Identify the blood parasite species.
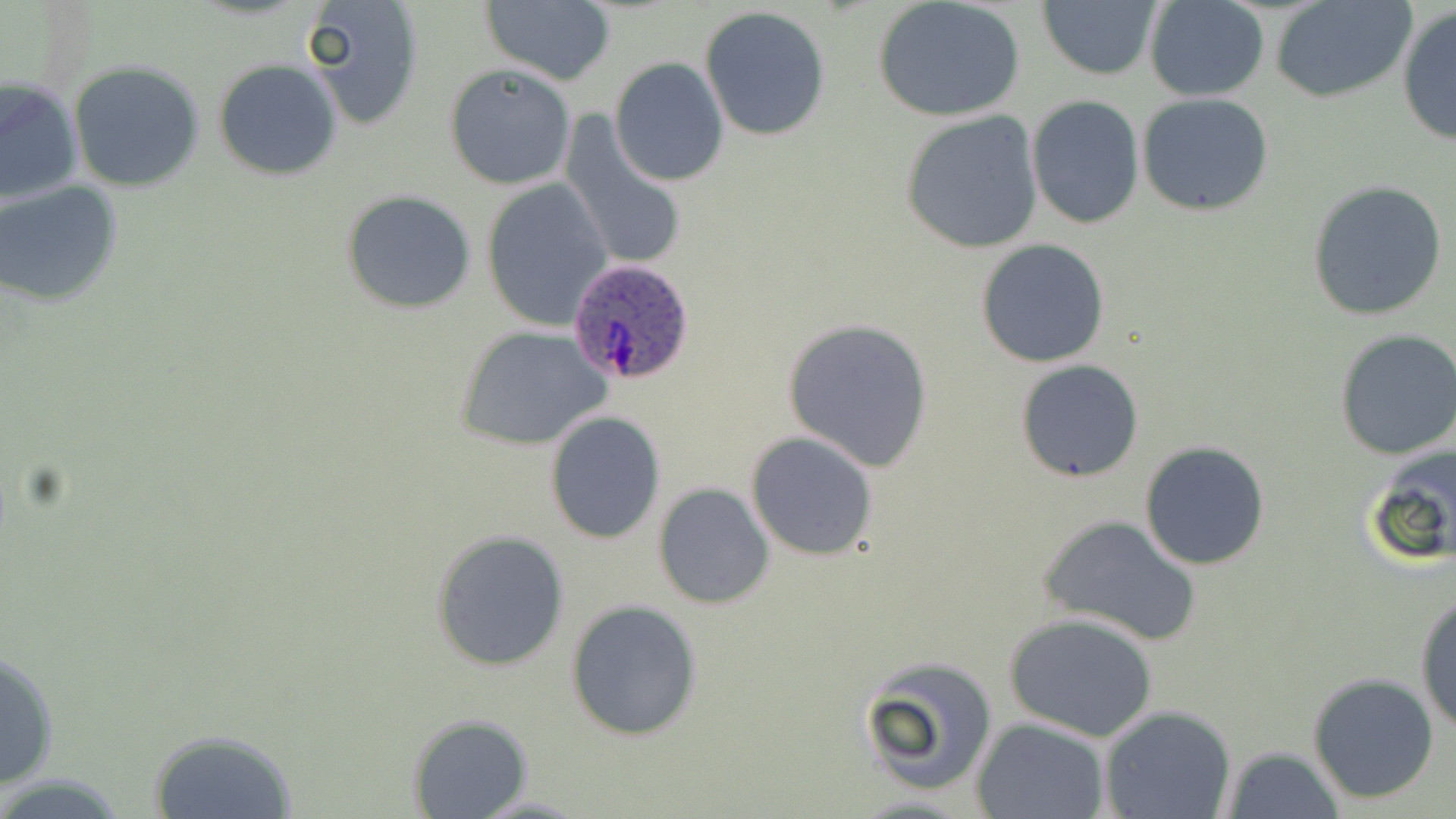

Plasmodium ovale.

Summary:
  - Coordinate format: approximate bounding boxes as [x1, y1, x2, y2] in pixels
  - Plasmodium ovale-infected red blood cell locations: [566, 257, 697, 386]
  - Uninfected red blood cell locations: [300, 0, 427, 131], [479, 0, 618, 87], [871, 0, 1027, 123], [1268, 0, 1420, 104], [1144, 1, 1271, 101], [1037, 2, 1161, 81], [699, 6, 832, 142], [1396, 7, 1456, 146], [610, 57, 729, 186], [213, 59, 342, 180], [68, 61, 205, 191], [444, 63, 579, 191], [0, 75, 84, 205], [1136, 91, 1275, 217], [1026, 97, 1145, 229], [899, 110, 1045, 253], [556, 112, 691, 276], [481, 178, 613, 330], [1305, 179, 1449, 321], [0, 180, 124, 309], [341, 189, 478, 315], [975, 238, 1110, 368], [782, 318, 934, 473], [454, 324, 611, 451], [1334, 330, 1456, 461], [1015, 359, 1143, 483], [544, 411, 667, 543], [745, 433, 879, 559], [1139, 441, 1272, 571], [1361, 442, 1456, 567], [653, 482, 776, 610], [1038, 514, 1204, 648], [430, 531, 570, 671], [1414, 591, 1456, 734], [566, 599, 704, 741], [1004, 612, 1158, 742], [1, 647, 60, 794], [858, 655, 998, 799], [1306, 671, 1439, 804], [1098, 705, 1238, 819], [406, 713, 532, 819], [973, 717, 1110, 819], [147, 728, 298, 818], [1219, 745, 1345, 819], [470, 793, 591, 817]
  - Image size: 1456×819 pixels
  - Magnification: 1000x
  - Field of view: single
  - Preparation: thin blood smear
  - Stain: May-Grünwald-Giemsa
  - Modality: optical microscopy